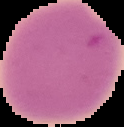
Summary:
  - Preparation: thin blood film
  - Image size: 124×127 pixels
  - Result: negative for malaria parasites
  - Image type: cell region segmented out of the field of view; surrounding area masked to black